Identify the parasite.
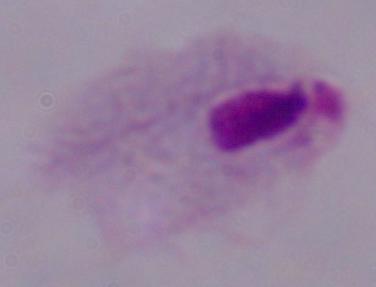
This is a trichomonad.

Summary:
  - Modality: micrograph
  - Magnification: 1000x